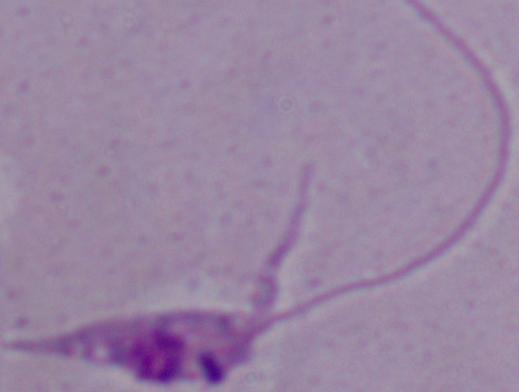 1000x magnification. Photomicrograph. A Leishmania parasite is seen.